Classify this cell by malaria status.
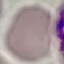
Uninfected.

Thin blood smear. Cell patch, automatically extracted from a larger field of view and resized to 64 × 64 pixels. Giemsa-stained preparation. Acquired by smartphone through the microscope eyepiece.